Assess this cell for malaria.
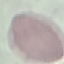
Uninfected.

image type = automatically extracted cell patch, resized to 64 × 64 pixels
preparation = thin blood film
capture = smartphone through the microscope eyepiece
stain = Giemsa